Describe the morphology of the red blood cells.
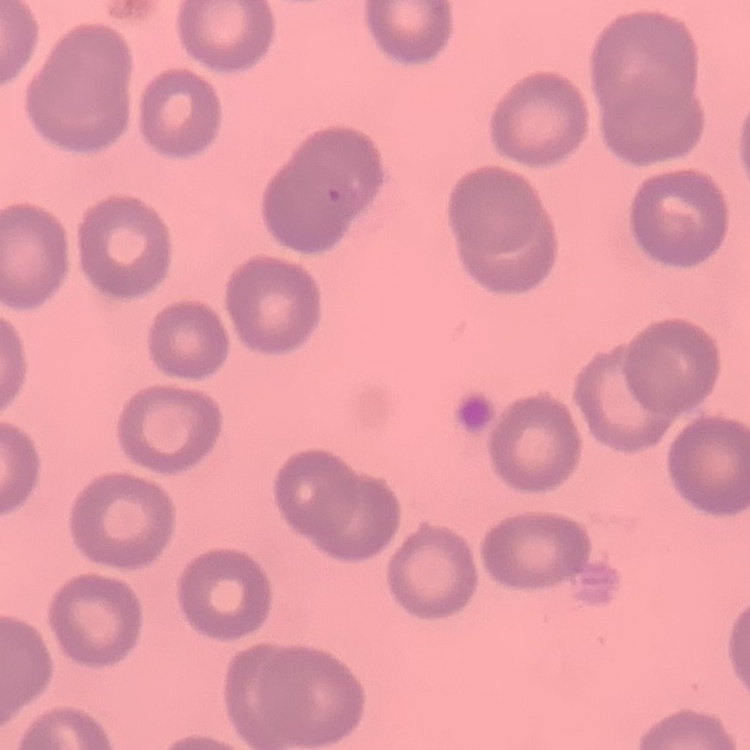
No rouleaux formation.

One tile cut from a larger photomicrograph. Thin blood film. Field's or Giemsa stain.